Locate every Plasmodium parasite.
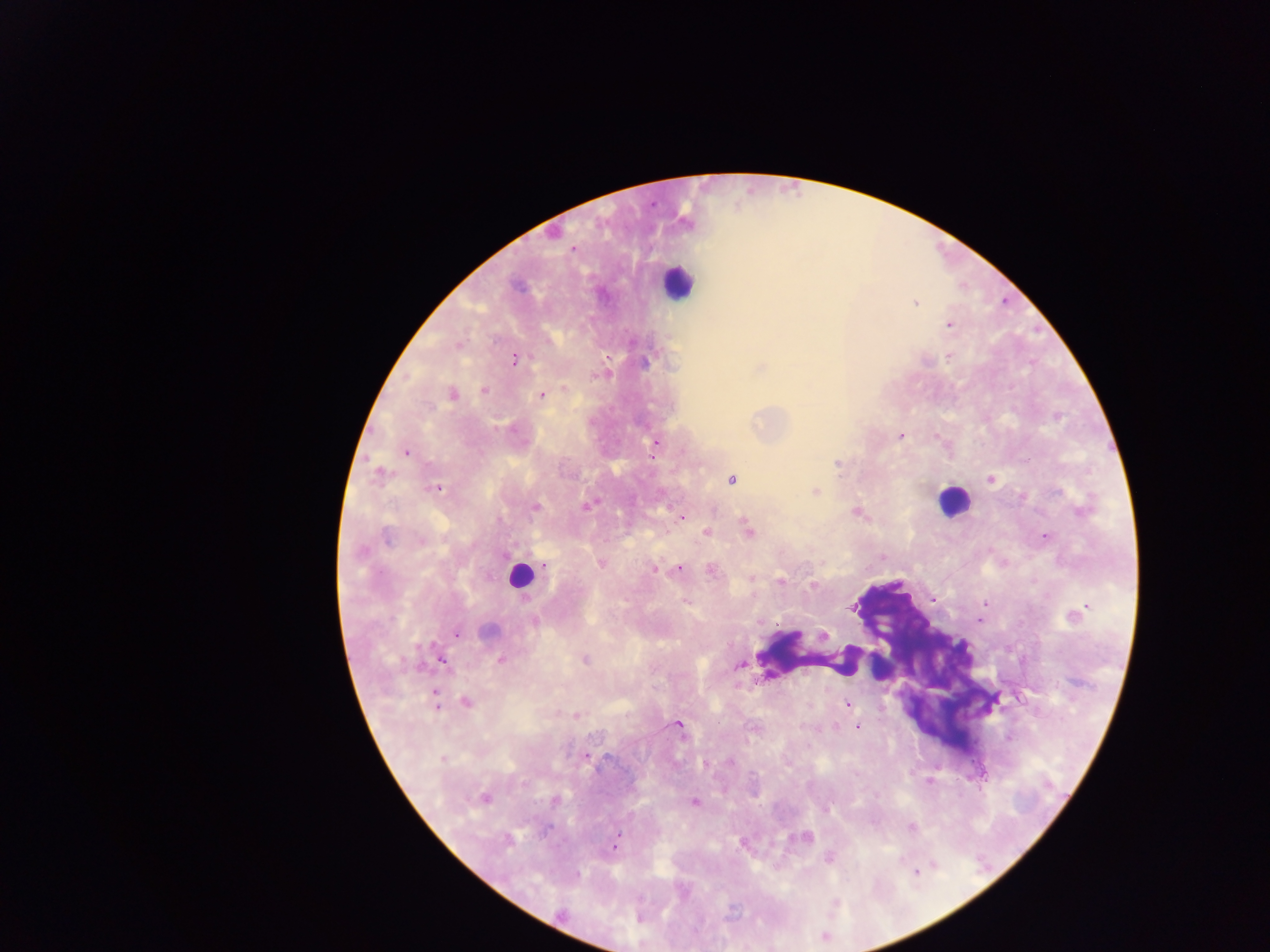
Approximate centers as {x, y} in pixels.
Plasmodium parasites: {572, 249}, {915, 303}, {949, 325}, {950, 357}, {515, 359}, {645, 362}, {565, 388}, {484, 390}, {452, 394}, {542, 395}, {511, 429}, {900, 436}, {655, 443}, {654, 451}, {406, 452}, {1027, 461}, {837, 464}, {380, 472}, {991, 479}, {732, 480}, {436, 488}, {815, 491}, {586, 505}, {535, 507}, {857, 512}, {683, 516}, {748, 530}, {707, 533}, {387, 536}, {1045, 537}, {421, 541}, {601, 563}, {545, 565}, {680, 569}, {654, 570}, {712, 571}, {752, 578}, {780, 580}, {813, 586}, {933, 598}, {984, 605}, {853, 608}, {1077, 614}, {980, 619}, {535, 621}, {489, 630}, {456, 634}, {824, 636}, {501, 660}, {585, 660}, {443, 661}, {739, 664}, {435, 698}, {466, 702}, {847, 704}, {576, 715}, {679, 725}, {857, 727}, {586, 756}, {442, 759}, {730, 762}, {485, 798}, {556, 801}, {695, 801}, {911, 826}, {545, 830}, {806, 838}, {508, 839}, {741, 843}, {616, 845}, {830, 859}, {916, 872}, {561, 913}.

capture = mobile-phone photograph through a microscope
country = Ghana
field of view = single
image size = 1270×952 pixels
preparation = thick blood smear
leukocyte locations = approximate centers as {x, y} in pixels: {678, 282}, {952, 501}, {520, 576}